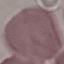
result = no malaria parasites seen
stain = Giemsa
capture = smartphone through the microscope eyepiece
image type = automatically extracted cell patch, resized to 64 × 64 pixels
preparation = thin smear